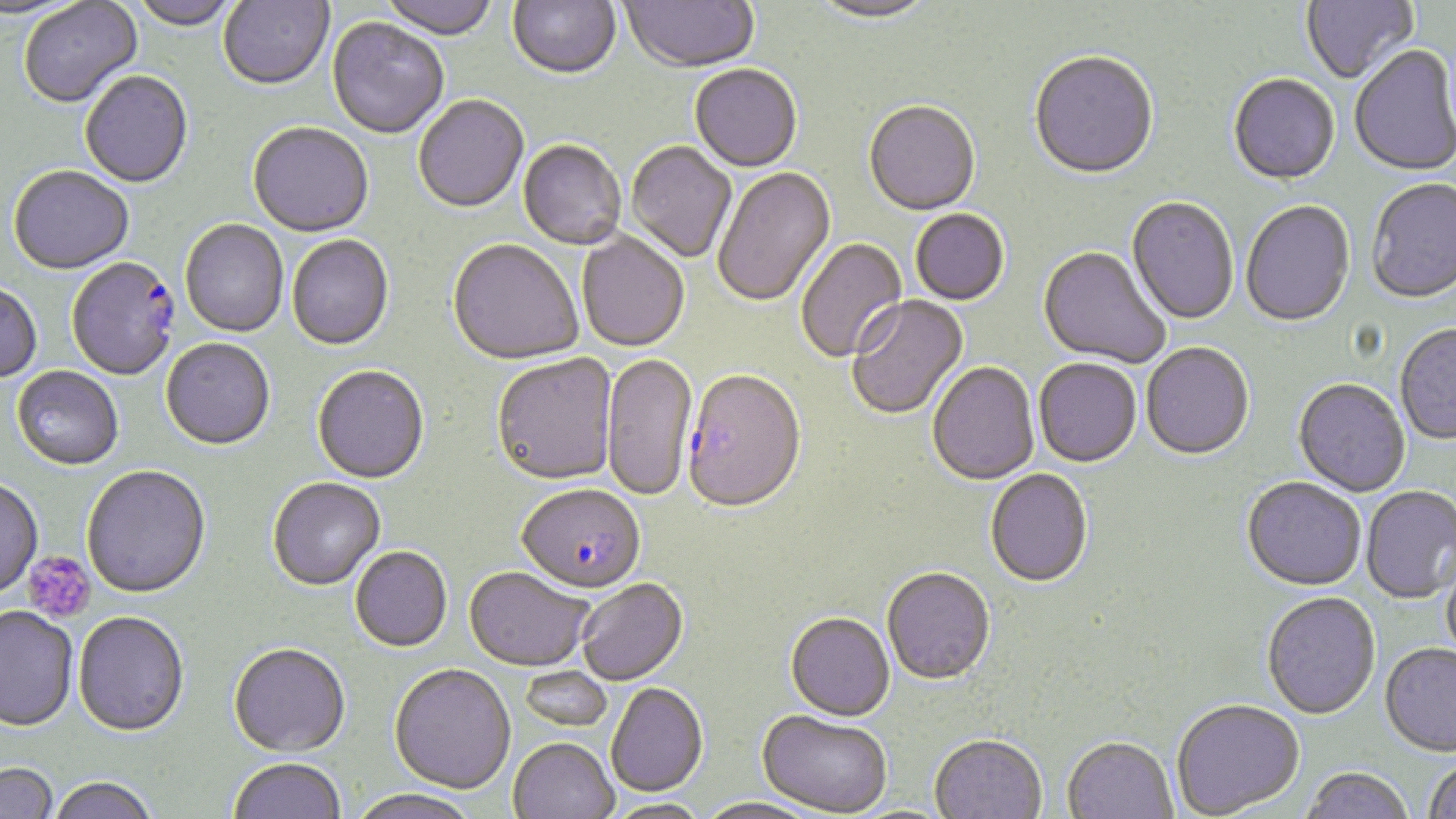

Summary:
  - Coordinate format: approximate bounding boxes as (x1, y1, x2, y2) in pixels
  - Plasmodium falciparum-infected red blood cell locations: (66, 260, 180, 382), (681, 373, 807, 517), (517, 485, 646, 597)
  - Uninfected red blood cell locations: (0, 0, 87, 23), (129, 0, 241, 32), (218, 0, 334, 92), (378, 0, 500, 42), (508, 0, 621, 82), (620, 0, 759, 75), (809, 0, 937, 26), (1301, 0, 1418, 86), (18, 2, 143, 110), (327, 19, 449, 141), (1350, 47, 1455, 178), (1029, 54, 1159, 182), (689, 66, 802, 174), (80, 73, 193, 190), (1228, 76, 1340, 187), (413, 97, 529, 216), (864, 103, 981, 218), (248, 124, 373, 239), (518, 141, 626, 251), (626, 142, 737, 264), (8, 167, 134, 277), (713, 168, 837, 308), (1366, 180, 1456, 306), (1126, 198, 1238, 326), (1241, 202, 1355, 329), (911, 210, 1009, 307), (180, 220, 288, 338), (577, 231, 689, 353), (287, 236, 394, 352), (796, 238, 908, 364), (446, 241, 582, 367), (1037, 247, 1170, 369), (0, 283, 42, 384), (847, 295, 969, 422), (1395, 326, 1456, 446), (161, 340, 275, 452), (1142, 344, 1254, 462), (602, 353, 697, 504), (492, 354, 618, 488), (1034, 360, 1142, 470), (927, 363, 1040, 487), (312, 367, 429, 486), (12, 368, 123, 471), (1293, 380, 1410, 498), (81, 466, 211, 600), (985, 470, 1093, 590), (0, 479, 43, 600), (268, 479, 386, 592), (1242, 479, 1366, 593), (1361, 487, 1456, 605), (350, 548, 452, 653), (1441, 556, 1456, 669), (464, 569, 595, 672), (882, 570, 995, 688), (577, 579, 688, 686), (1262, 594, 1381, 721), (0, 606, 79, 732), (73, 613, 189, 738), (785, 614, 895, 724), (228, 645, 350, 759), (1380, 645, 1456, 759), (389, 666, 516, 796), (518, 666, 613, 732), (605, 684, 709, 798), (1172, 701, 1304, 819), (757, 712, 891, 817), (930, 737, 1046, 818), (508, 738, 619, 819), (1062, 739, 1178, 819), (229, 759, 345, 818), (1423, 761, 1456, 819), (0, 763, 59, 819), (1300, 769, 1414, 819), (49, 777, 158, 819), (347, 790, 481, 819), (603, 799, 711, 819), (694, 799, 824, 819)
  - Platelet locations: (23, 551, 96, 624)
  - Slide-level diagnosis: Plasmodium falciparum
  - Image size: 1456×819 pixels
  - Field of view: single
  - Modality: optical microscopy
  - Stain: May-Grünwald-Giemsa
  - Magnification: 1000x
  - Preparation: thin blood smear